State which parasite is depicted.
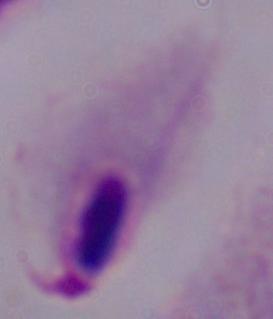
A trichomonad.

Micrograph. 1000x magnification.